Locate every malaria parasite and identify its life-cycle stage.
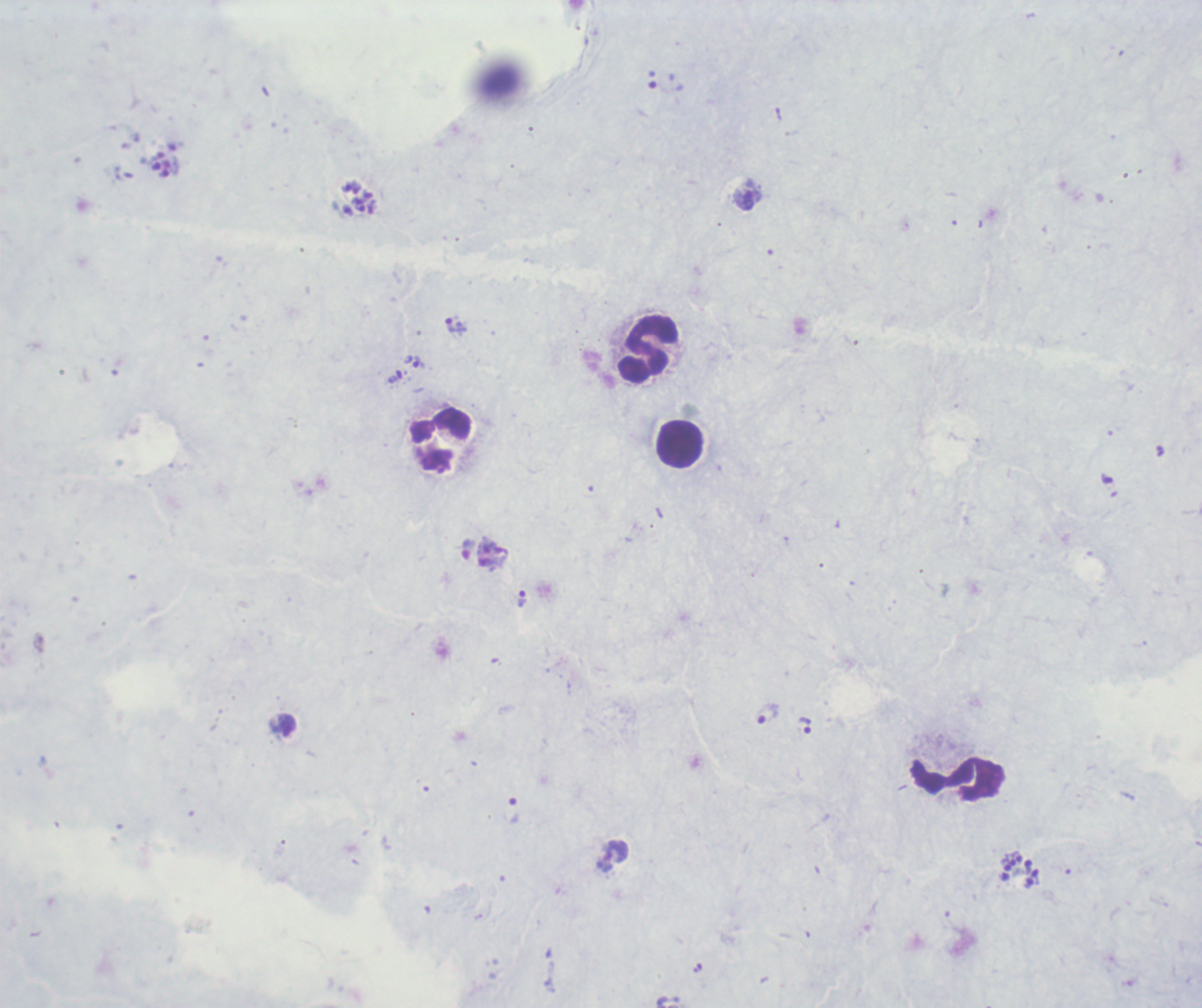

Approximate centers as (x, y) in pixels.
Trophozoites: (747, 199), (456, 326), (419, 363), (395, 377), (486, 546), (522, 599), (768, 714), (285, 725), (805, 725), (513, 811), (616, 852).
Schizonts: (161, 164), (360, 197), (1020, 869).
No gametocyte forms observed.

Approximate centers as (x, y) in pixels. Leukocyte locations: (648, 348), (442, 441), (681, 445), (957, 780). Previously used in a real diagnosis. Image is 1202×1008 pixels. Romanowsky stain. Captured at 100x magnification. Background quality: poor. Thick blood smear. Single field of view.